Assess this cell for malaria.
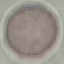

It is uninfected.

Thin smear of blood. Automatically extracted cell patch, resized to 64 × 64 pixels. Photographed with a smartphone camera at the microscope eyepiece. Giemsa stain.